Give the extent of all uninfected red blood cells.
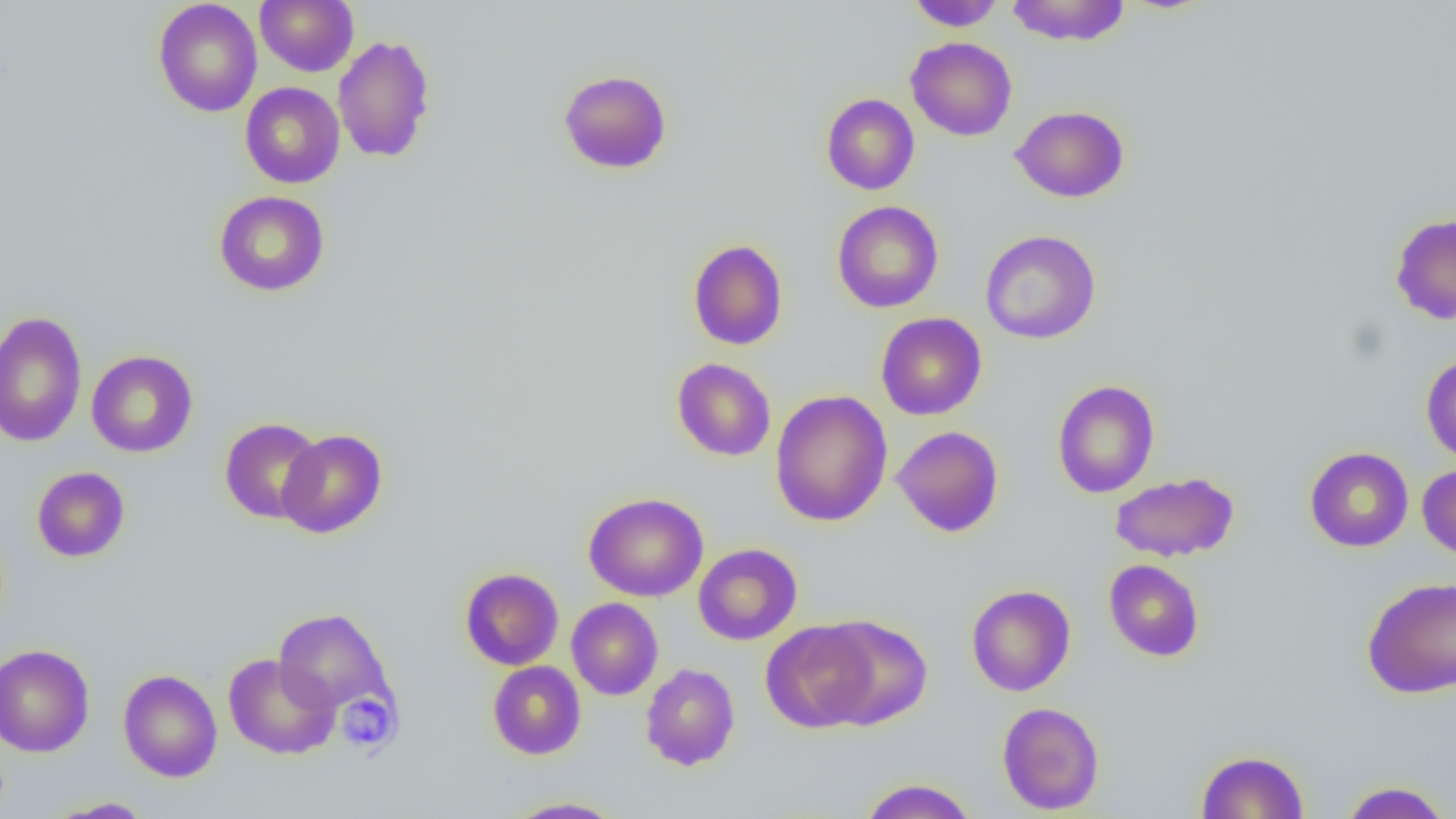
Approximate bounding boxes as named x1/y1/x2/y2 corners in pixels.
Uninfected red blood cells: (x1=153, y1=0, x2=263, y2=117), (x1=255, y1=0, x2=358, y2=76), (x1=907, y1=0, x2=1005, y2=31), (x1=1005, y1=0, x2=1130, y2=47), (x1=332, y1=34, x2=436, y2=163), (x1=906, y1=37, x2=1017, y2=141), (x1=558, y1=69, x2=672, y2=174), (x1=240, y1=82, x2=345, y2=188), (x1=821, y1=93, x2=919, y2=195), (x1=1010, y1=105, x2=1129, y2=203), (x1=213, y1=190, x2=330, y2=296), (x1=832, y1=200, x2=943, y2=313), (x1=1389, y1=214, x2=1456, y2=325), (x1=980, y1=229, x2=1101, y2=344), (x1=688, y1=239, x2=788, y2=350), (x1=0, y1=311, x2=88, y2=447), (x1=876, y1=312, x2=987, y2=420), (x1=86, y1=350, x2=198, y2=457), (x1=1421, y1=354, x2=1456, y2=465), (x1=672, y1=358, x2=776, y2=461), (x1=1051, y1=379, x2=1160, y2=498), (x1=770, y1=389, x2=893, y2=527), (x1=220, y1=418, x2=324, y2=524), (x1=892, y1=426, x2=1004, y2=536), (x1=277, y1=429, x2=387, y2=538), (x1=1304, y1=447, x2=1413, y2=552), (x1=1417, y1=464, x2=1456, y2=562), (x1=31, y1=466, x2=130, y2=562), (x1=1110, y1=471, x2=1240, y2=562), (x1=583, y1=492, x2=709, y2=602), (x1=693, y1=543, x2=802, y2=645), (x1=1104, y1=559, x2=1204, y2=662), (x1=460, y1=567, x2=564, y2=670), (x1=1362, y1=576, x2=1456, y2=698), (x1=966, y1=584, x2=1076, y2=696), (x1=567, y1=597, x2=663, y2=700), (x1=273, y1=607, x2=397, y2=719), (x1=814, y1=615, x2=933, y2=730), (x1=762, y1=620, x2=879, y2=733), (x1=0, y1=644, x2=95, y2=757), (x1=222, y1=653, x2=340, y2=759), (x1=487, y1=661, x2=586, y2=759), (x1=640, y1=663, x2=740, y2=771), (x1=118, y1=669, x2=223, y2=782), (x1=996, y1=701, x2=1105, y2=815), (x1=1197, y1=750, x2=1308, y2=818), (x1=858, y1=778, x2=978, y2=819), (x1=1338, y1=780, x2=1453, y2=819), (x1=504, y1=796, x2=626, y2=818), (x1=45, y1=797, x2=153, y2=818).

Summary:
  - Platelet locations: (x1=337, y1=693, x2=397, y2=752)
  - Slide-level diagnosis: negative for blood parasites
  - Field of view: single
  - Image size: 1456×819 pixels
  - Magnification: 1000x
  - Modality: light microscopy
  - Preparation: thin blood film